Outline each blood parasite and name the species.
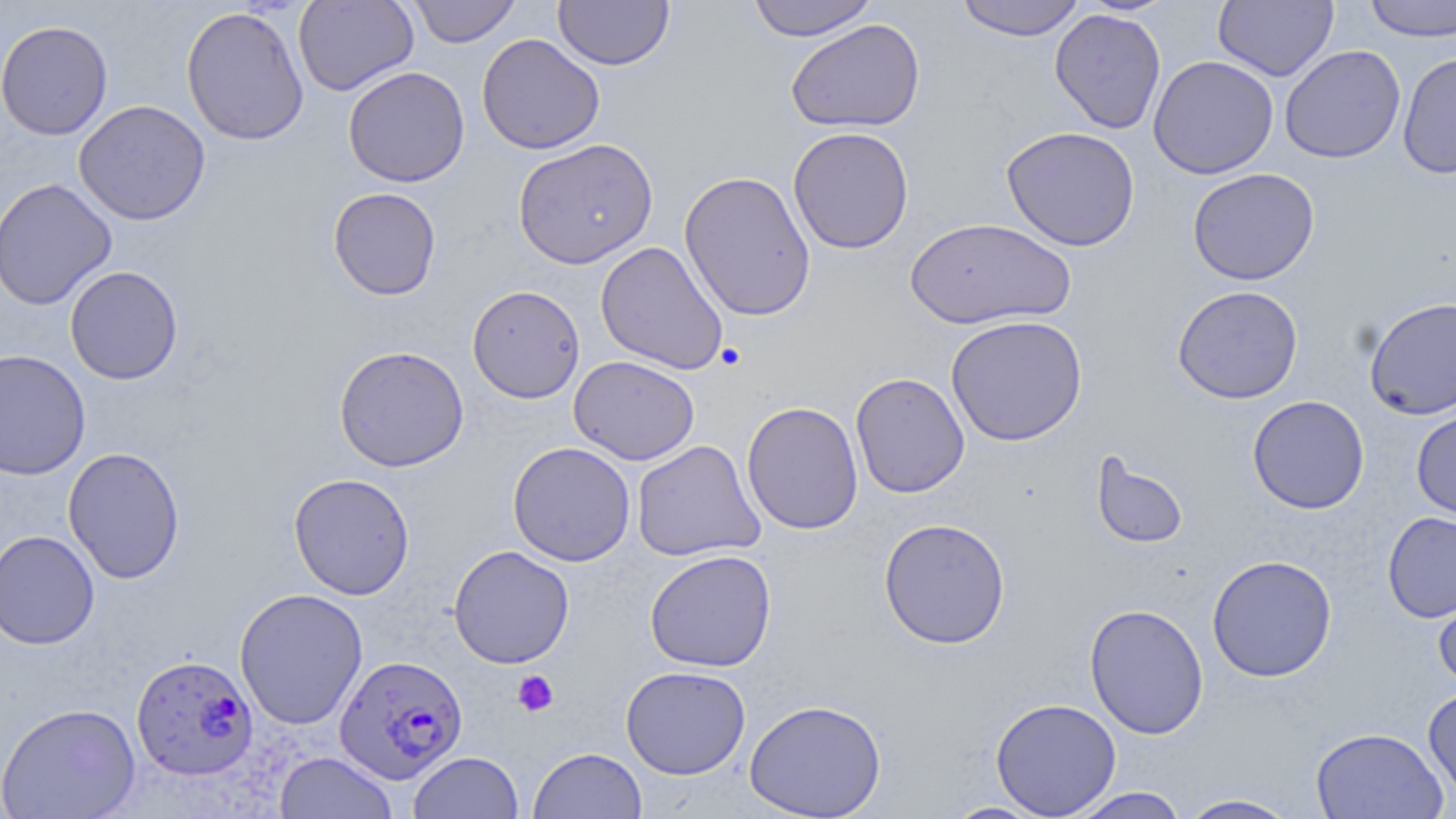
Approximate bounding boxes as named x1/y1/x2/y2 corners in pixels.
Plasmodium falciparum-infected red blood cells: (x1=131, y1=653, x2=258, y2=780), (x1=335, y1=654, x2=468, y2=784).
No Plasmodium ovale, Plasmodium malariae, Plasmodium vivax, Babesia divergens, or Trypanosoma brucei observed.

slide_level_diagnosis: Plasmodium falciparum
preparation: thin blood smear
stain: May-Grünwald-Giemsa
platelet_locations: 'approximate bounding boxes as named x1/y1/x2/y2 corners in pixels: (x1=513, y1=670, x2=559, y2=716)'
modality: light microscopy
image_size: 1456×819 pixels
magnification: 1000x
field_of_view: single
uninfected_red_blood_cell_locations: 'approximate bounding boxes as named x1/y1/x2/y2 corners in pixels: (x1=293, y1=0, x2=419, y2=96), (x1=407, y1=0, x2=523, y2=47), (x1=553, y1=0, x2=675, y2=70), (x1=746, y1=0, x2=879, y2=41), (x1=954, y1=0, x2=1086, y2=41), (x1=1214, y1=0, x2=1338, y2=82), (x1=1362, y1=0, x2=1456, y2=43), (x1=181, y1=6, x2=309, y2=146), (x1=1049, y1=8, x2=1166, y2=134), (x1=0, y1=19, x2=113, y2=141), (x1=785, y1=19, x2=925, y2=134), (x1=476, y1=33, x2=605, y2=155), (x1=1279, y1=45, x2=1405, y2=164), (x1=1397, y1=51, x2=1456, y2=179), (x1=1147, y1=55, x2=1279, y2=179), (x1=342, y1=66, x2=470, y2=187), (x1=74, y1=100, x2=211, y2=225), (x1=787, y1=126, x2=914, y2=255), (x1=1001, y1=126, x2=1141, y2=251), (x1=512, y1=138, x2=658, y2=269), (x1=1188, y1=168, x2=1319, y2=285), (x1=679, y1=170, x2=817, y2=322), (x1=0, y1=177, x2=117, y2=310), (x1=328, y1=187, x2=442, y2=300), (x1=904, y1=217, x2=1075, y2=330), (x1=595, y1=241, x2=729, y2=375), (x1=65, y1=265, x2=183, y2=384), (x1=467, y1=284, x2=585, y2=404), (x1=1172, y1=285, x2=1303, y2=405), (x1=1363, y1=296, x2=1456, y2=420), (x1=946, y1=315, x2=1088, y2=446), (x1=333, y1=345, x2=470, y2=472), (x1=0, y1=348, x2=91, y2=481), (x1=569, y1=355, x2=700, y2=465), (x1=850, y1=372, x2=970, y2=498), (x1=1247, y1=395, x2=1370, y2=514), (x1=741, y1=401, x2=864, y2=535), (x1=1411, y1=405, x2=1456, y2=522), (x1=631, y1=440, x2=765, y2=563), (x1=507, y1=441, x2=636, y2=566), (x1=62, y1=446, x2=185, y2=584), (x1=1091, y1=452, x2=1188, y2=549), (x1=288, y1=473, x2=416, y2=600), (x1=1382, y1=511, x2=1456, y2=623), (x1=878, y1=517, x2=1011, y2=650), (x1=0, y1=530, x2=101, y2=650), (x1=448, y1=545, x2=575, y2=669), (x1=644, y1=550, x2=777, y2=672), (x1=1206, y1=554, x2=1337, y2=682), (x1=1433, y1=579, x2=1456, y2=692), (x1=234, y1=587, x2=368, y2=729), (x1=1084, y1=603, x2=1209, y2=739), (x1=620, y1=665, x2=751, y2=779), (x1=1423, y1=686, x2=1456, y2=801), (x1=990, y1=697, x2=1122, y2=818), (x1=743, y1=698, x2=887, y2=819), (x1=0, y1=702, x2=141, y2=819), (x1=1310, y1=726, x2=1449, y2=819), (x1=528, y1=747, x2=648, y2=819), (x1=274, y1=751, x2=398, y2=818), (x1=409, y1=751, x2=524, y2=819), (x1=1066, y1=787, x2=1190, y2=818), (x1=1177, y1=794, x2=1301, y2=818), (x1=942, y1=801, x2=1050, y2=818)'